Locate platelets.
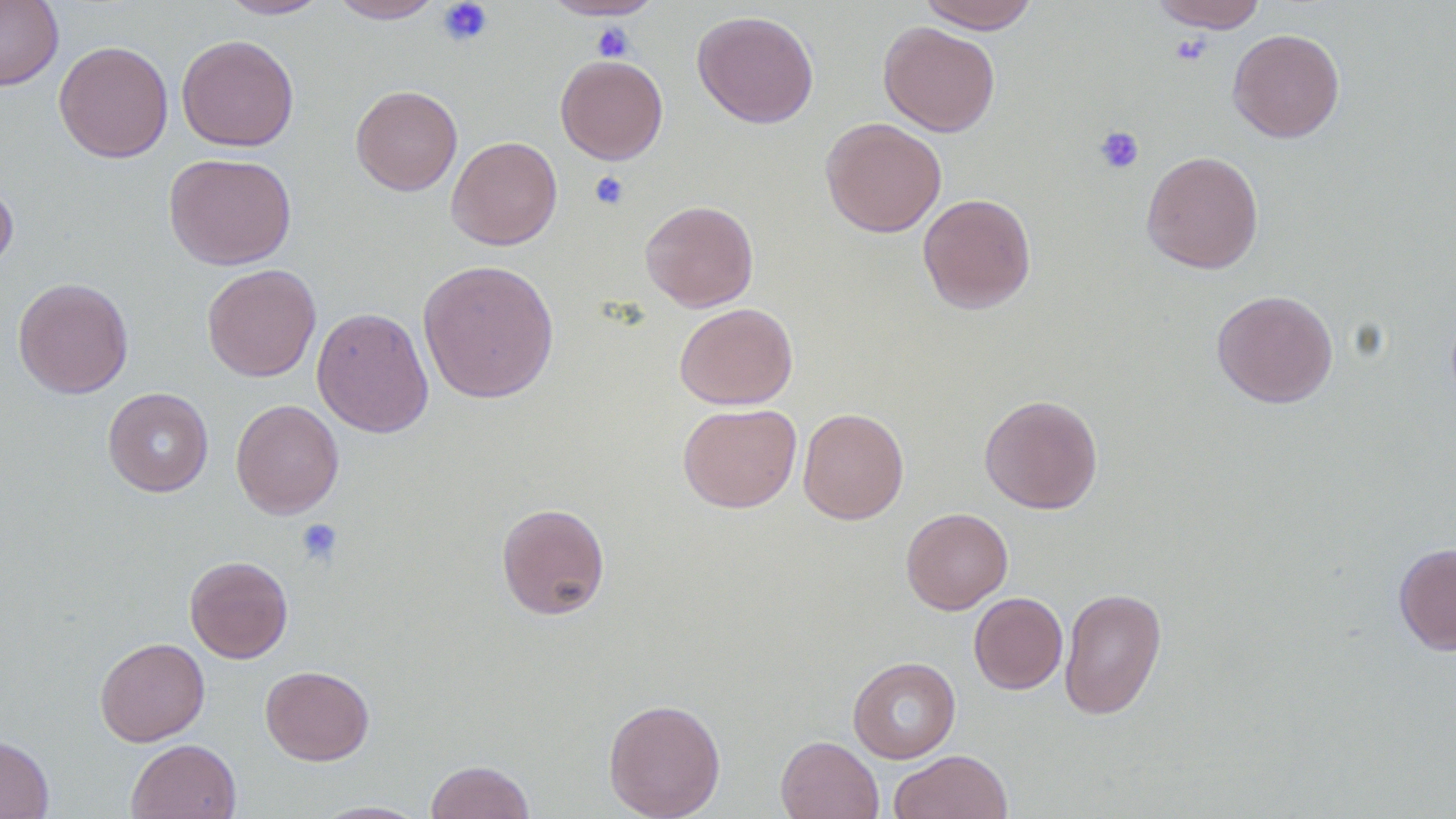

Approximate bounding boxes as named x1/y1/x2/y2 corners in pixels.
Platelets: (x1=436, y1=1, x2=494, y2=47), (x1=590, y1=22, x2=635, y2=61), (x1=1170, y1=34, x2=1212, y2=66), (x1=1094, y1=126, x2=1144, y2=175), (x1=589, y1=170, x2=630, y2=210), (x1=296, y1=518, x2=343, y2=566).

Uninfected red blood cell locations: (x1=0, y1=0, x2=63, y2=90), (x1=219, y1=0, x2=331, y2=19), (x1=328, y1=0, x2=445, y2=23), (x1=542, y1=0, x2=663, y2=20), (x1=916, y1=0, x2=1041, y2=33), (x1=1149, y1=1, x2=1267, y2=32), (x1=692, y1=10, x2=819, y2=128), (x1=879, y1=22, x2=1000, y2=136), (x1=1227, y1=28, x2=1345, y2=143), (x1=176, y1=34, x2=299, y2=152), (x1=54, y1=41, x2=173, y2=163), (x1=555, y1=54, x2=668, y2=164), (x1=350, y1=85, x2=462, y2=196), (x1=820, y1=117, x2=946, y2=237), (x1=446, y1=136, x2=562, y2=250), (x1=1141, y1=150, x2=1264, y2=274), (x1=163, y1=152, x2=297, y2=270), (x1=0, y1=174, x2=18, y2=278), (x1=918, y1=193, x2=1036, y2=313), (x1=640, y1=199, x2=758, y2=312), (x1=418, y1=259, x2=559, y2=403), (x1=202, y1=264, x2=321, y2=382), (x1=13, y1=277, x2=133, y2=399), (x1=1211, y1=289, x2=1338, y2=408), (x1=674, y1=302, x2=798, y2=410), (x1=311, y1=307, x2=434, y2=438), (x1=103, y1=388, x2=214, y2=497), (x1=979, y1=394, x2=1103, y2=514), (x1=230, y1=399, x2=344, y2=519), (x1=678, y1=403, x2=802, y2=513), (x1=798, y1=407, x2=909, y2=525), (x1=496, y1=502, x2=611, y2=620), (x1=901, y1=507, x2=1013, y2=614), (x1=1393, y1=542, x2=1456, y2=655), (x1=184, y1=555, x2=294, y2=663), (x1=1059, y1=587, x2=1167, y2=720), (x1=969, y1=592, x2=1068, y2=694), (x1=95, y1=637, x2=209, y2=746), (x1=848, y1=656, x2=961, y2=763), (x1=261, y1=665, x2=374, y2=765), (x1=603, y1=698, x2=726, y2=818), (x1=0, y1=734, x2=54, y2=819), (x1=775, y1=735, x2=884, y2=819), (x1=126, y1=738, x2=242, y2=819), (x1=888, y1=750, x2=1013, y2=819), (x1=425, y1=760, x2=535, y2=819), (x1=310, y1=800, x2=430, y2=818). Slide-level diagnosis: negative for blood parasites. Light microscopy. Thin blood film. Single field of view. Image is 1456×819 pixels. 1000x magnification.